State which parasite is depicted.
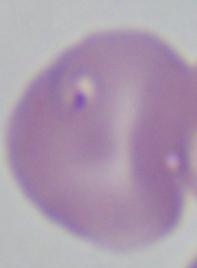

This is Babesia.

modality: micrograph
magnification: 1000x